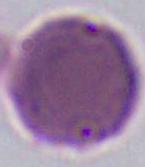
{
  "modality": "micrograph",
  "identification": "erythrocyte",
  "magnification": "1000x"
}